Identify the parasite.
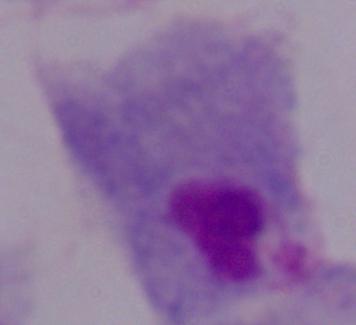

This is a trichomonad.

Captured at 1000x magnification. Micrograph.